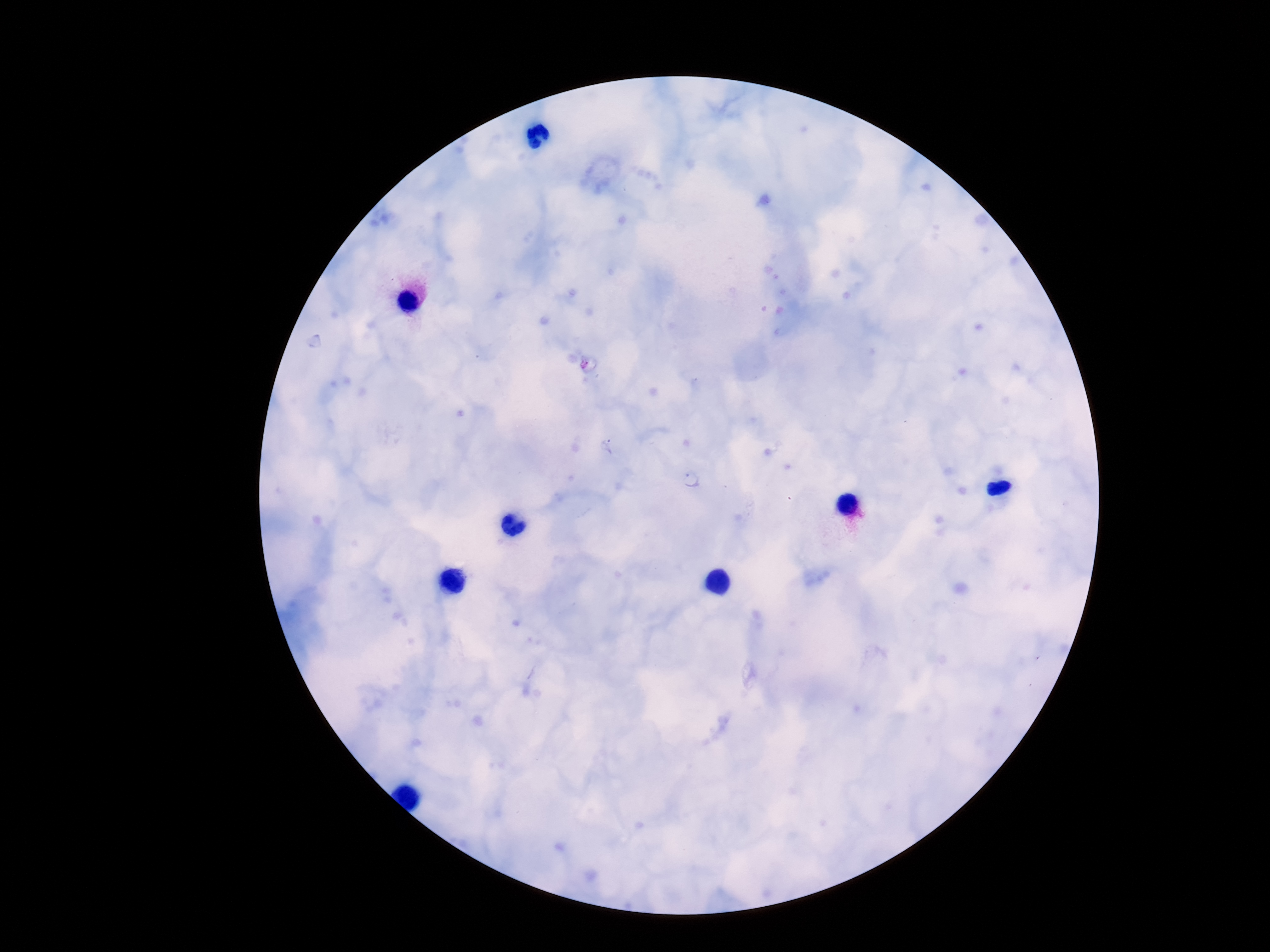 Approximate centers as (x, y) in pixels. Plasmodium parasite locations: (608, 445), (690, 480). Photographed through the microscope eyepiece with a smartphone camera. 100x magnification. Image is 1270×952 pixels. Patient malaria status: positive. Thick blood smear. Giemsa-stained preparation. One field from this slide.